Describe the morphology of the erythrocytes.
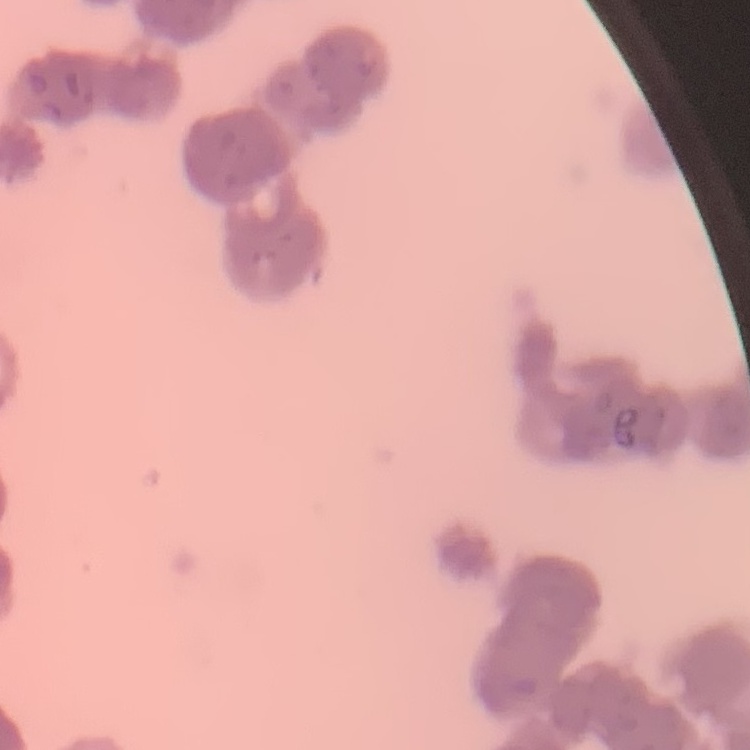

They show rouleaux formation.

image_type: square crop of a larger photomicrograph
stain: Field's or Giemsa
preparation: thin peripheral smear